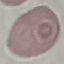
malaria status = uninfected
image type = cell patch, automatically extracted from a larger field of view and resized to 64 × 64 pixels
stain = Giemsa
capture = smartphone camera at the microscope eyepiece
preparation = thin blood smear